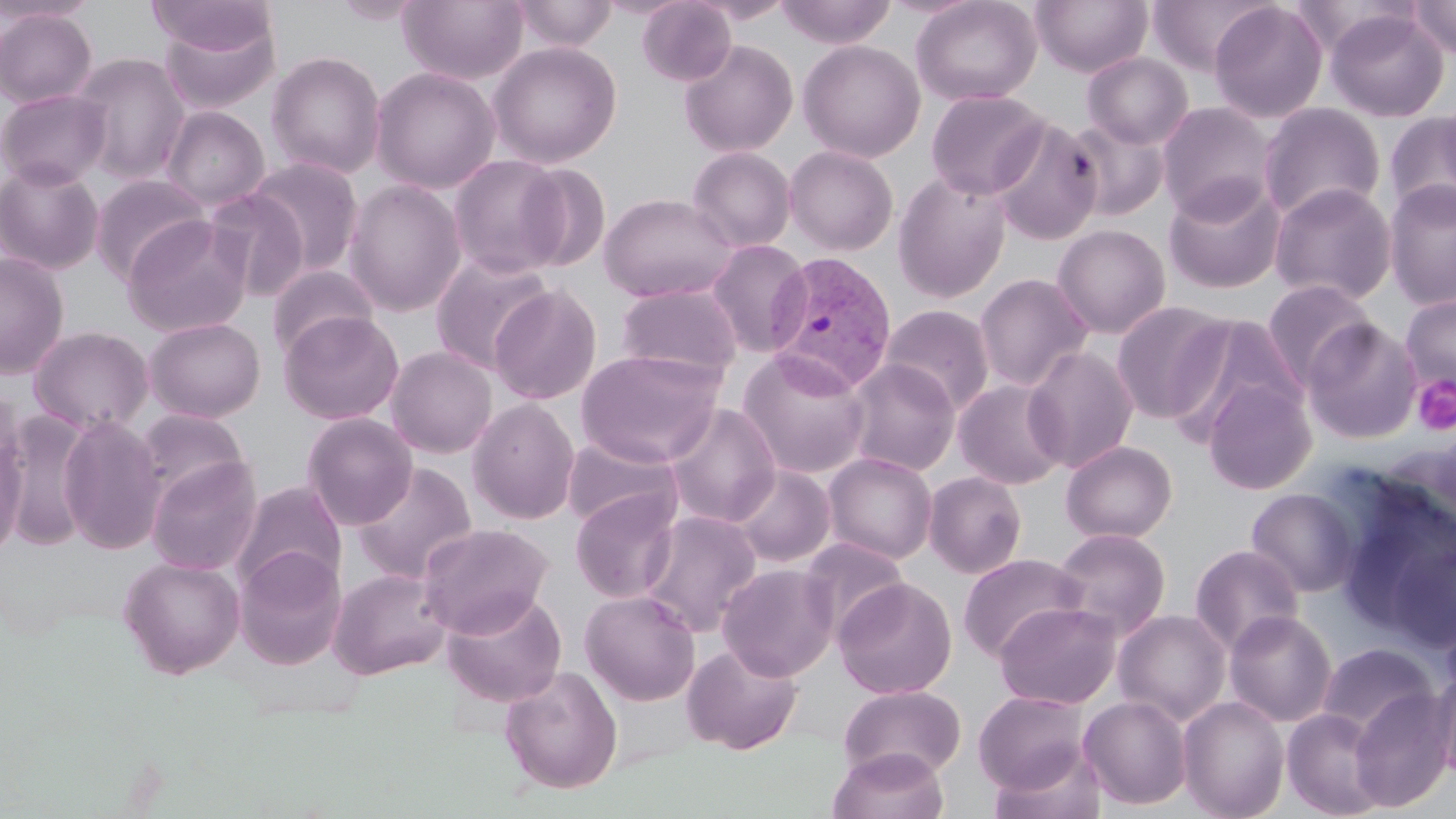

Summary:
  - Coordinate format: approximate bounding boxes as named x1/y1/x2/y2 corners in pixels
  - Platelet locations: (x1=1413, y1=376, x2=1456, y2=435)
  - Plasmodium vivax-infected red blood cell locations: (x1=765, y1=251, x2=898, y2=394)
  - Uninfected red blood cell locations: (x1=0, y1=0, x2=99, y2=23), (x1=146, y1=0, x2=275, y2=59), (x1=333, y1=0, x2=425, y2=25), (x1=398, y1=0, x2=528, y2=84), (x1=511, y1=0, x2=619, y2=52), (x1=637, y1=0, x2=736, y2=86), (x1=775, y1=0, x2=896, y2=47), (x1=911, y1=0, x2=1043, y2=106), (x1=1031, y1=0, x2=1153, y2=76), (x1=1148, y1=0, x2=1274, y2=76), (x1=1408, y1=0, x2=1456, y2=60), (x1=1209, y1=2, x2=1328, y2=123), (x1=0, y1=7, x2=98, y2=108), (x1=1325, y1=8, x2=1449, y2=122), (x1=157, y1=14, x2=281, y2=115), (x1=678, y1=39, x2=798, y2=157), (x1=798, y1=40, x2=926, y2=162), (x1=488, y1=42, x2=622, y2=168), (x1=266, y1=50, x2=386, y2=179), (x1=71, y1=52, x2=191, y2=183), (x1=1082, y1=52, x2=1194, y2=149), (x1=371, y1=66, x2=500, y2=193), (x1=0, y1=88, x2=111, y2=190), (x1=925, y1=89, x2=1049, y2=200), (x1=1436, y1=94, x2=1456, y2=200), (x1=1157, y1=101, x2=1277, y2=222), (x1=1258, y1=102, x2=1386, y2=222), (x1=162, y1=106, x2=269, y2=210), (x1=1385, y1=112, x2=1456, y2=222), (x1=1064, y1=116, x2=1171, y2=221), (x1=989, y1=117, x2=1103, y2=246), (x1=784, y1=145, x2=899, y2=255), (x1=687, y1=147, x2=796, y2=253), (x1=448, y1=154, x2=570, y2=278), (x1=247, y1=157, x2=364, y2=275), (x1=0, y1=161, x2=105, y2=275), (x1=516, y1=162, x2=611, y2=272), (x1=892, y1=171, x2=1012, y2=303), (x1=90, y1=173, x2=211, y2=285), (x1=1163, y1=177, x2=1287, y2=293), (x1=344, y1=180, x2=466, y2=317), (x1=1384, y1=180, x2=1456, y2=309), (x1=1268, y1=182, x2=1397, y2=305), (x1=202, y1=187, x2=311, y2=300), (x1=598, y1=193, x2=737, y2=303), (x1=122, y1=216, x2=254, y2=338), (x1=1052, y1=224, x2=1171, y2=338), (x1=706, y1=239, x2=812, y2=357), (x1=0, y1=251, x2=69, y2=379), (x1=430, y1=252, x2=554, y2=374), (x1=266, y1=265, x2=379, y2=362), (x1=973, y1=273, x2=1093, y2=392), (x1=1262, y1=279, x2=1378, y2=390), (x1=614, y1=282, x2=742, y2=381), (x1=488, y1=285, x2=602, y2=405), (x1=1400, y1=293, x2=1456, y2=396), (x1=1111, y1=301, x2=1231, y2=423), (x1=881, y1=304, x2=995, y2=414), (x1=279, y1=311, x2=403, y2=425), (x1=1165, y1=314, x2=1303, y2=441), (x1=144, y1=317, x2=266, y2=422), (x1=1302, y1=320, x2=1421, y2=444), (x1=29, y1=326, x2=153, y2=435), (x1=1022, y1=346, x2=1139, y2=473), (x1=386, y1=347, x2=498, y2=458), (x1=575, y1=349, x2=725, y2=467), (x1=737, y1=349, x2=871, y2=479), (x1=843, y1=359, x2=960, y2=476), (x1=1204, y1=378, x2=1316, y2=496), (x1=954, y1=379, x2=1068, y2=490), (x1=467, y1=397, x2=580, y2=525), (x1=664, y1=403, x2=781, y2=527), (x1=135, y1=409, x2=250, y2=503), (x1=4, y1=412, x2=96, y2=551), (x1=302, y1=413, x2=417, y2=529), (x1=58, y1=415, x2=166, y2=554), (x1=561, y1=434, x2=683, y2=533), (x1=0, y1=436, x2=26, y2=561), (x1=1061, y1=440, x2=1177, y2=543), (x1=823, y1=453, x2=938, y2=564), (x1=146, y1=456, x2=262, y2=576), (x1=353, y1=463, x2=477, y2=583), (x1=729, y1=464, x2=836, y2=568), (x1=924, y1=471, x2=1027, y2=579), (x1=232, y1=481, x2=347, y2=593), (x1=1333, y1=484, x2=1455, y2=641), (x1=1246, y1=488, x2=1362, y2=597), (x1=570, y1=489, x2=682, y2=603), (x1=639, y1=511, x2=762, y2=636), (x1=418, y1=523, x2=553, y2=637), (x1=1052, y1=528, x2=1170, y2=640), (x1=800, y1=536, x2=910, y2=637), (x1=1386, y1=538, x2=1456, y2=655), (x1=1190, y1=544, x2=1304, y2=655), (x1=234, y1=547, x2=346, y2=670), (x1=958, y1=553, x2=1087, y2=661), (x1=119, y1=556, x2=245, y2=679), (x1=717, y1=563, x2=838, y2=681), (x1=328, y1=568, x2=451, y2=679), (x1=833, y1=577, x2=956, y2=699), (x1=441, y1=590, x2=567, y2=707), (x1=579, y1=590, x2=701, y2=706), (x1=994, y1=601, x2=1121, y2=709), (x1=1113, y1=609, x2=1232, y2=726), (x1=1224, y1=610, x2=1337, y2=727), (x1=1439, y1=610, x2=1456, y2=704), (x1=681, y1=642, x2=802, y2=755), (x1=1316, y1=642, x2=1438, y2=739), (x1=499, y1=665, x2=623, y2=795), (x1=1432, y1=665, x2=1456, y2=785), (x1=838, y1=684, x2=966, y2=781), (x1=1348, y1=687, x2=1455, y2=812), (x1=974, y1=690, x2=1090, y2=794), (x1=1079, y1=695, x2=1192, y2=810), (x1=1178, y1=696, x2=1290, y2=819), (x1=1281, y1=708, x2=1388, y2=818), (x1=986, y1=742, x2=1109, y2=819), (x1=829, y1=747, x2=949, y2=819)
  - Slide-level diagnosis: Plasmodium vivax
  - Magnification: 1000x
  - Preparation: thin blood smear
  - Image size: 1456×819 pixels
  - Stain: May-Grünwald-Giemsa
  - Field of view: single
  - Modality: optical microscopy